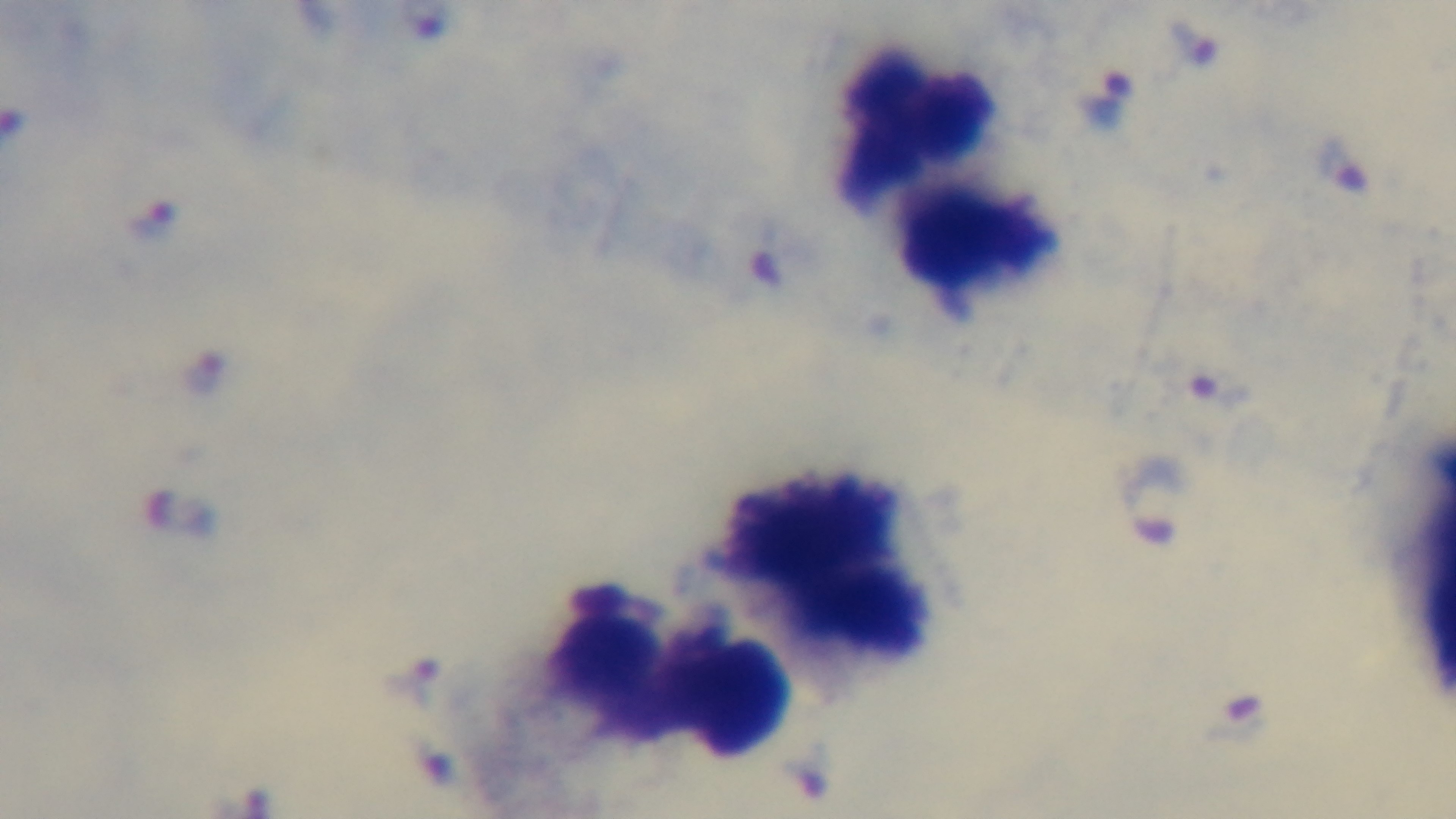
modality: light microscopy
capture: mounted 4K digital camera
objective: 100x oil immersion
preparation: thick blood film
malaria_status: positive
stain: Giemsa
field_of_view: one from the slide